Describe the morphology of the erythrocytes.
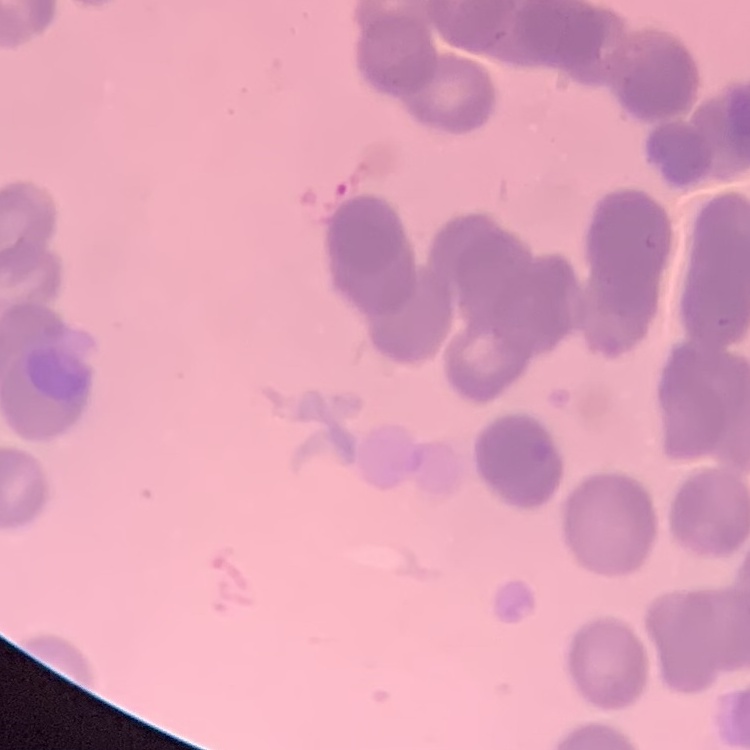

Rouleaux formation.

Summary:
  - Image type: square crop of a larger photomicrograph
  - Preparation: thin blood film
  - Stain: Field's or Giemsa